Describe the morphology of the erythrocytes.
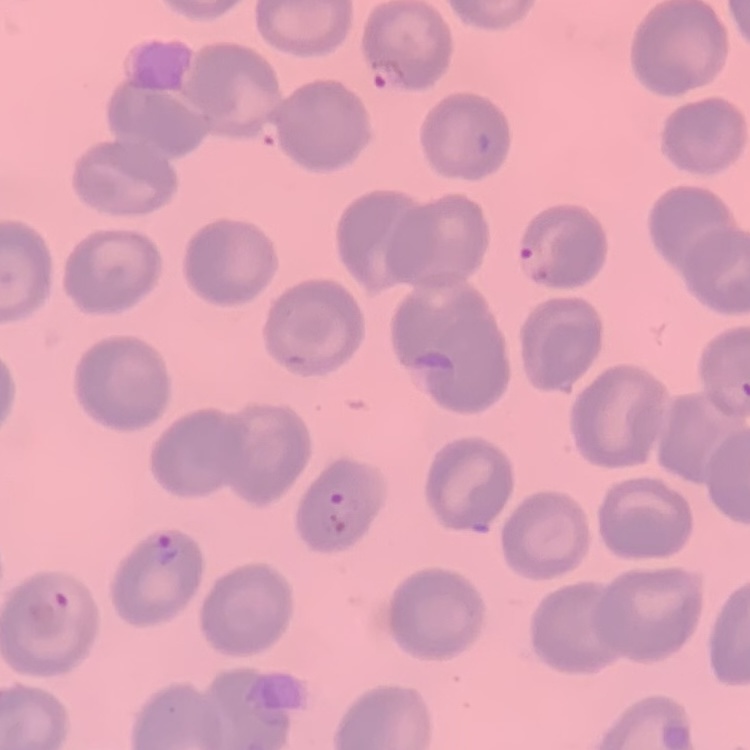

No rouleaux formation.

Thin blood smear. Square crop of a larger photomicrograph. Field's or Giemsa stain.